Identify the parasite.
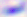

This is Toxoplasma gondii.

{
  "modality": "photomicrograph",
  "magnification": "400x"
}